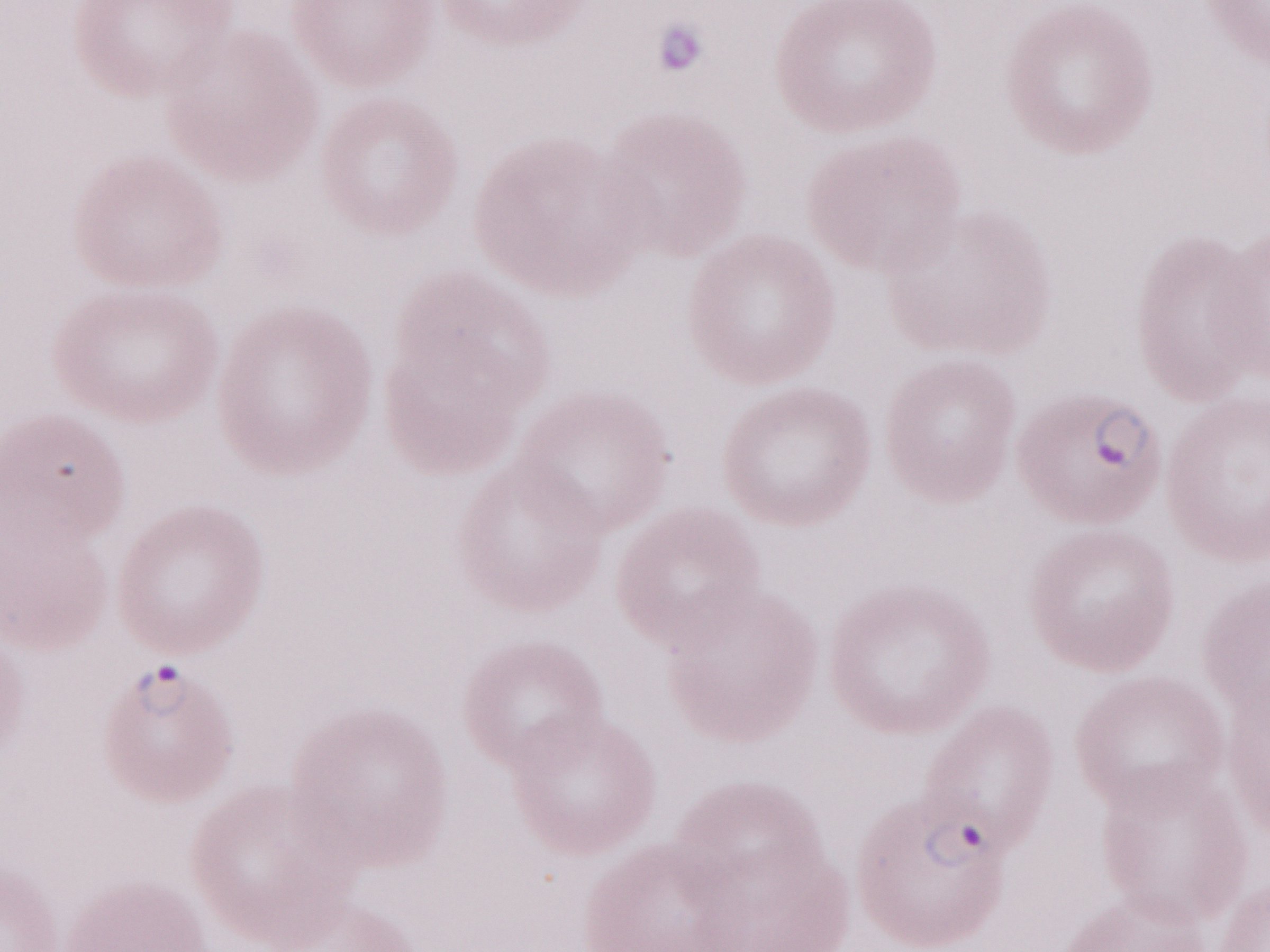 Thin peripheral-blood smear. May-Grünwald-Giemsa-stained preparation. Single field of view. Magnification: 1,000x. Olympus BX43 microscope and DP73 digital camera. Patient-level malaria diagnosis: positive. Image is 1270×952 pixels.